Assess this cell for malaria.
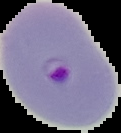
It is parasitized.

From a thin blood film. The area outside the segmented cell region is set to black. Image is 121×133 pixels.